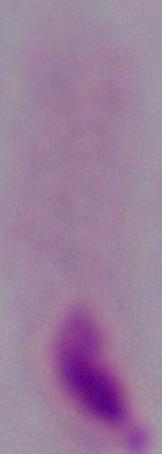
magnification: 1000x
modality: micrograph
identification: trichomonad